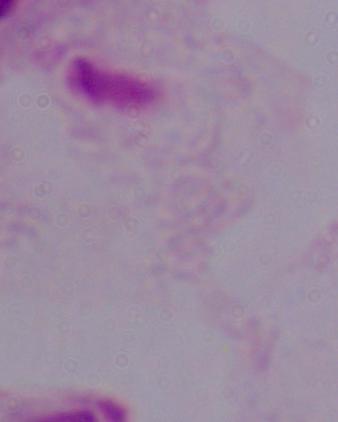

Captured at 1000x magnification. Micrograph. A trichomonad is seen.